Comment on the morphology of the erythrocytes.
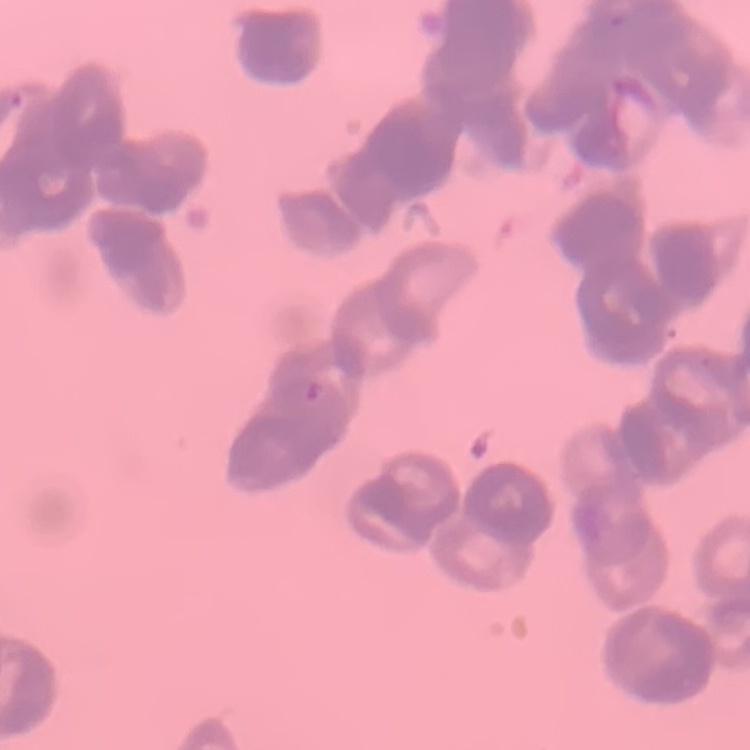
Rouleaux formation.

Summary:
  - Preparation: thin blood film
  - Image type: one tile cut from a larger photomicrograph
  - Stain: Field's or Giemsa